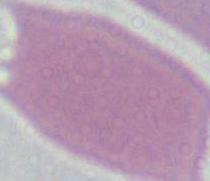

identification = erythrocyte
modality = photomicrograph
magnification = 1000x